State the blood parasite species.
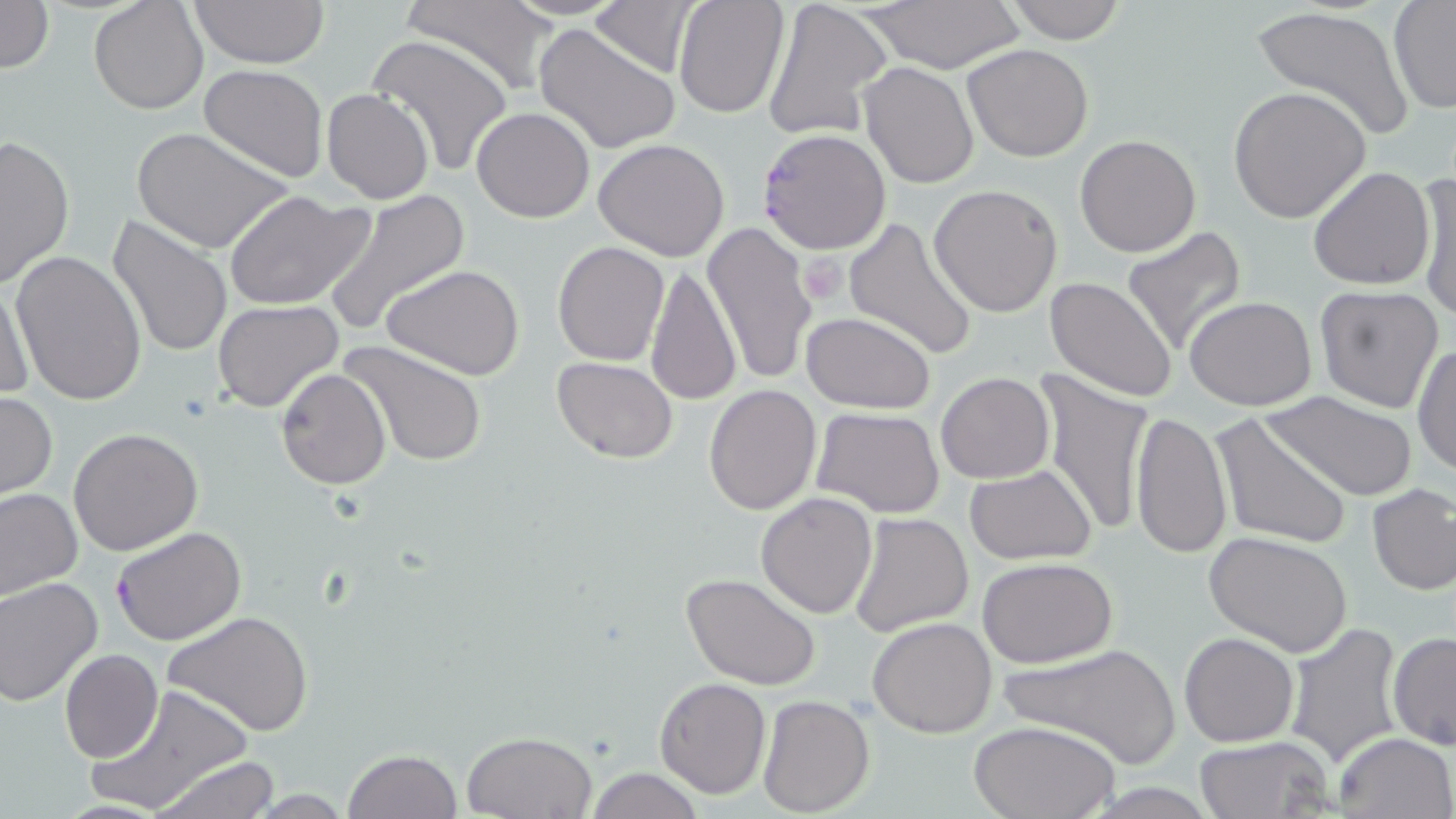
Plasmodium falciparum.

Summary:
  - Coordinate format: approximate bounding boxes as (x1,y1)-(x2,y2) corner pairs in pixels
  - Plasmodium falciparum-infected red blood cell locations: (757,129)-(892,255), (110,526)-(246,646)
  - Platelet locations: (798,254)-(847,305)
  - Uninfected red blood cell locations: (0,0)-(53,75), (89,0)-(208,114), (189,0)-(330,68), (402,0)-(557,92), (672,0)-(790,119), (761,0)-(890,141), (857,0)-(1027,71), (1003,0)-(1131,43), (1387,1)-(1456,114), (589,2)-(698,79), (1249,3)-(1418,144), (533,24)-(682,156), (365,34)-(514,177), (961,43)-(1094,164), (859,62)-(978,189), (199,64)-(328,182), (1228,85)-(1371,224), (323,89)-(433,204), (471,106)-(596,223), (130,126)-(295,255), (0,134)-(74,289), (1075,134)-(1201,258), (593,138)-(731,261), (1308,166)-(1436,291), (1415,170)-(1455,324), (929,184)-(1063,318), (322,190)-(470,335), (224,191)-(375,311), (107,216)-(232,359), (843,216)-(979,361), (702,223)-(818,390), (1120,227)-(1248,356), (553,241)-(671,366), (9,250)-(148,405), (645,262)-(740,406), (381,265)-(524,381), (1045,276)-(1179,401), (0,279)-(36,406), (1313,285)-(1445,415), (1185,295)-(1317,410), (212,299)-(344,413), (801,312)-(935,414), (342,341)-(490,466), (1413,342)-(1456,479), (552,357)-(678,462), (275,367)-(390,490), (1035,368)-(1156,540), (935,372)-(1054,484), (702,384)-(822,515), (0,390)-(57,501), (1259,390)-(1419,503), (813,407)-(947,517), (1130,409)-(1232,559), (1208,414)-(1355,552), (68,427)-(205,556), (964,465)-(1097,564), (1366,484)-(1456,597), (0,487)-(82,601), (756,491)-(878,618), (847,512)-(975,637), (1205,529)-(1356,659), (866,535)-(1030,663), (976,557)-(1119,668), (681,572)-(823,692), (0,577)-(102,707), (162,609)-(313,737), (868,617)-(998,738), (1283,621)-(1403,767), (1179,631)-(1299,747), (1388,631)-(1456,751), (995,643)-(1184,766), (60,648)-(164,763), (654,677)-(770,799), (83,684)-(257,816), (757,694)-(876,818), (970,719)-(1120,818), (460,730)-(596,817), (1333,732)-(1456,819), (1194,736)-(1334,819), (342,749)-(463,819), (149,756)-(283,818), (582,768)-(705,819)
  - Magnification: 1000x
  - Stain: May-Grünwald-Giemsa
  - Preparation: thin blood film
  - Image size: 1456×819 pixels
  - Modality: optical microscopy
  - Field of view: single